Assess the morphology of the red blood cells.
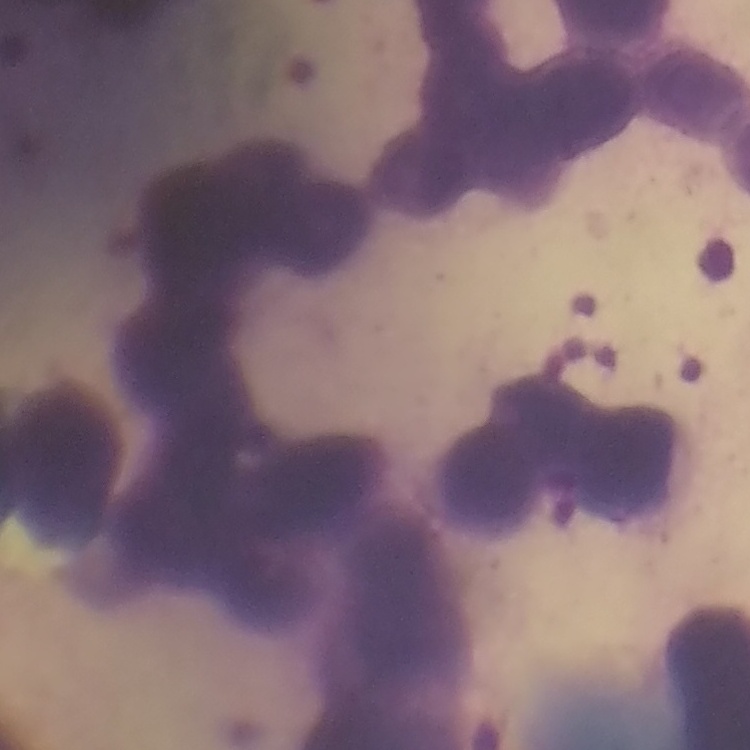

They show rouleaux formation.

image type = one tile cut from a larger photomicrograph
stain = Field's or Giemsa
preparation = thin blood smear